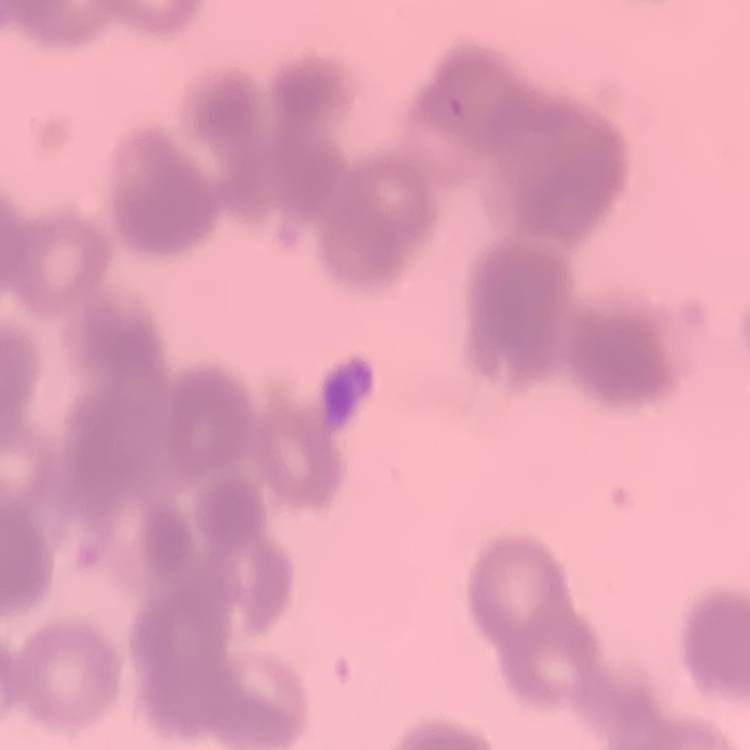
The red blood cells exhibit rouleaux formation. Field's or Giemsa stain. Square crop of a larger photomicrograph. Thin peripheral smear.